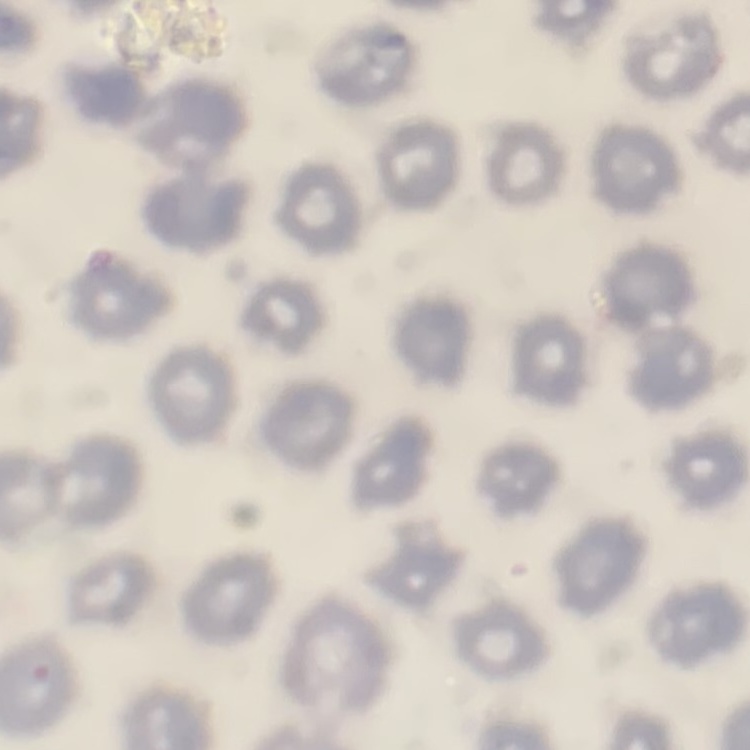
erythrocyte_morphology: no rouleaux formation
preparation: thin blood smear
stain: Field's or Giemsa
image_type: square crop of a larger photomicrograph